State which parasite is depicted.
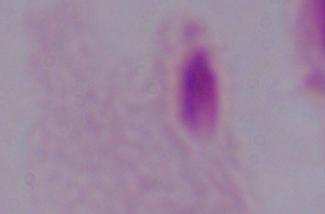
This is a trichomonad.

Summary:
  - Modality: micrograph
  - Magnification: 1000x